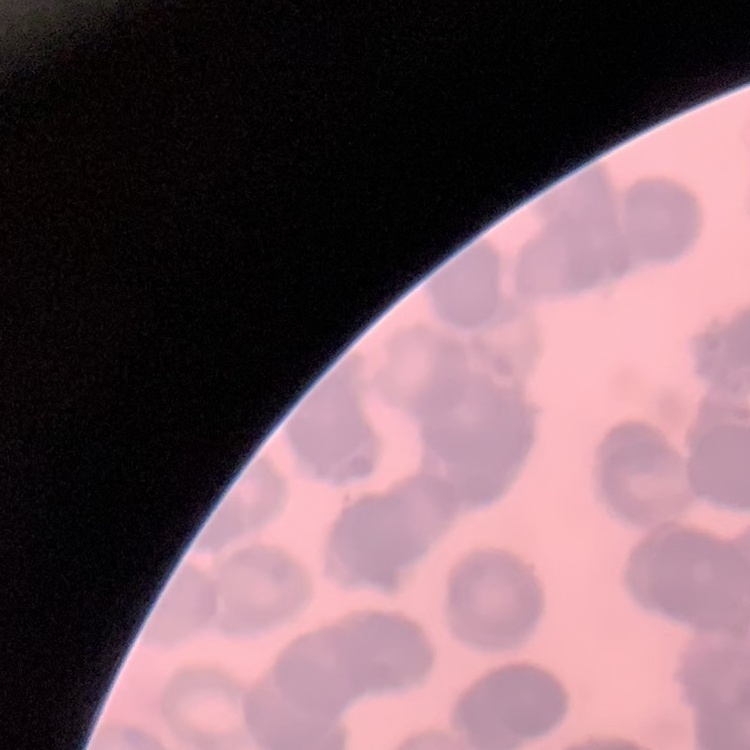

erythrocyte morphology = rouleaux formation
preparation = thin blood film
image type = square crop of a larger photomicrograph
stain = Field's or Giemsa